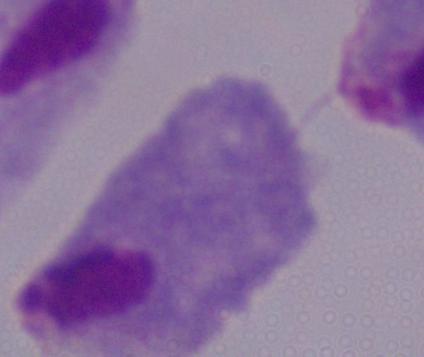 Captured at 1000x magnification. A trichomonad is shown. Photomicrograph.